Comment on the morphology of the red blood cells.
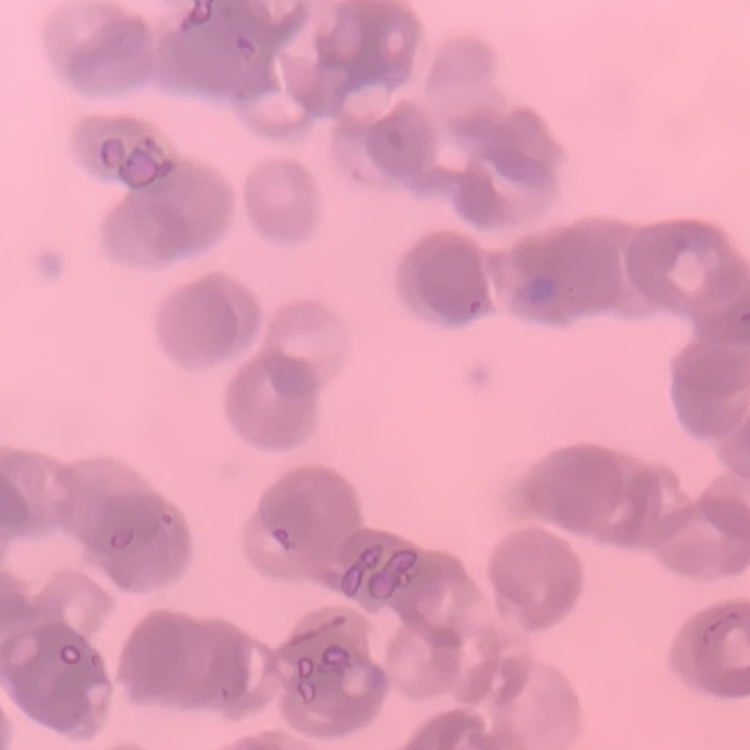
They show rouleaux formation.

stain = Field's or Giemsa
image type = one tile cut from a larger photomicrograph
preparation = thin peripheral smear